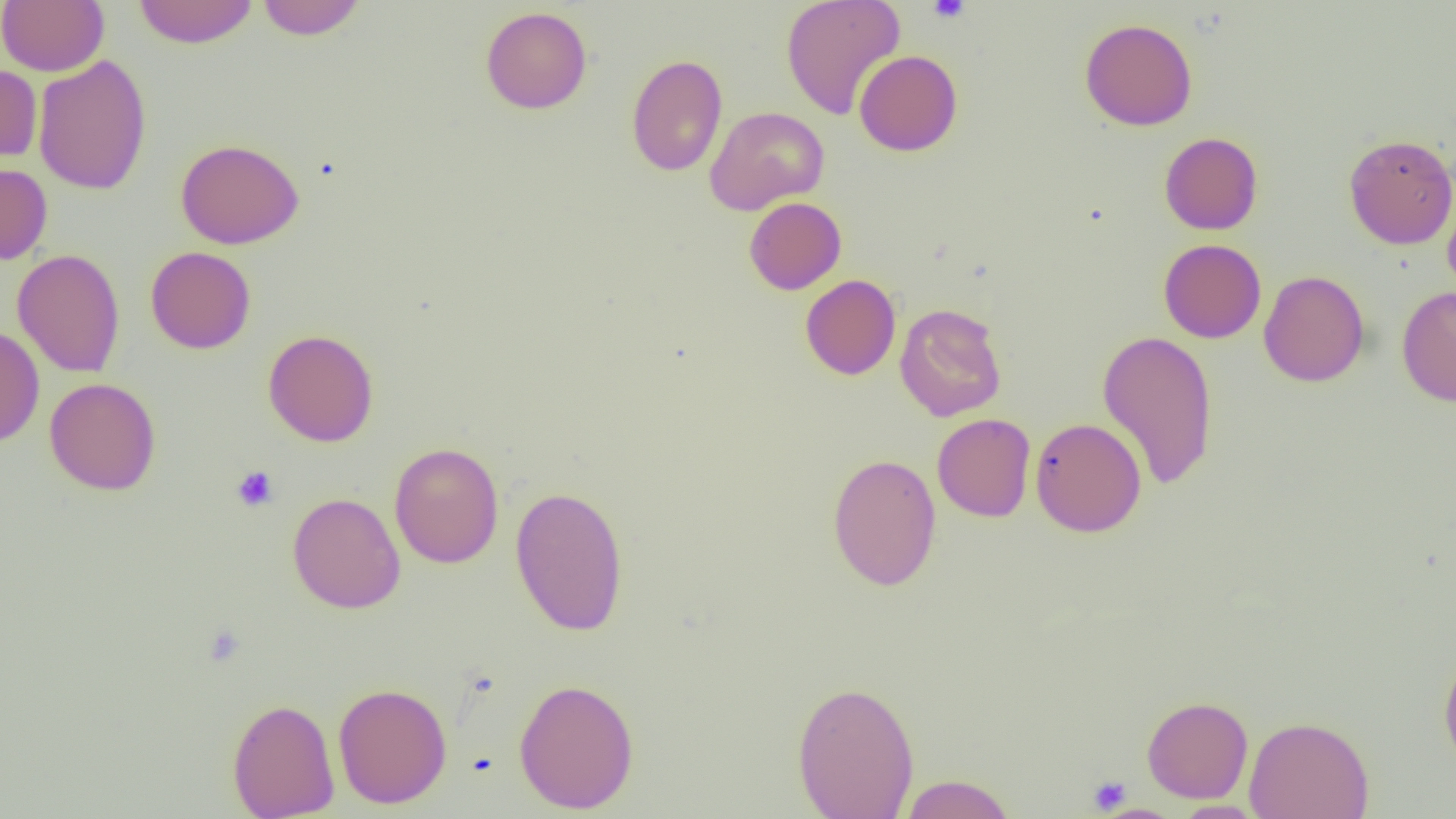
Summary:
  - Coordinate format: approximate bounding boxes as [x1, y1, x2, y2] in pixels
  - Uninfected red blood cell locations: [0, 0, 108, 75], [256, 0, 367, 40], [781, 0, 905, 119], [133, 1, 259, 48], [480, 6, 592, 114], [1079, 18, 1197, 131], [854, 50, 962, 156], [32, 54, 152, 195], [626, 54, 728, 176], [0, 64, 42, 164], [704, 106, 829, 215], [1159, 132, 1263, 235], [1343, 134, 1456, 249], [175, 138, 304, 249], [0, 162, 52, 265], [1442, 183, 1456, 300], [744, 197, 846, 295], [1158, 239, 1266, 343], [145, 246, 256, 354], [12, 249, 126, 378], [1259, 269, 1370, 387], [800, 274, 901, 380], [1396, 285, 1456, 407], [894, 303, 1007, 421], [0, 325, 44, 447], [263, 329, 379, 446], [1097, 329, 1218, 490], [44, 377, 161, 495], [932, 413, 1035, 522], [1031, 417, 1146, 537], [388, 441, 504, 569], [827, 453, 942, 590], [510, 485, 629, 636], [287, 492, 406, 614], [1439, 651, 1456, 771], [513, 677, 640, 813], [792, 680, 920, 819], [332, 682, 452, 809], [1141, 695, 1253, 803], [226, 697, 340, 819], [1244, 715, 1374, 819], [899, 774, 1016, 819], [1171, 799, 1267, 818], [1096, 804, 1186, 819]
  - Platelet locations: [927, 0, 970, 23], [231, 466, 279, 511], [1088, 775, 1131, 814]
  - Slide-level diagnosis: negative for blood parasites
  - Preparation: thin blood film
  - Field of view: single
  - Modality: optical microscopy
  - Magnification: 1000x
  - Image size: 1456×819 pixels